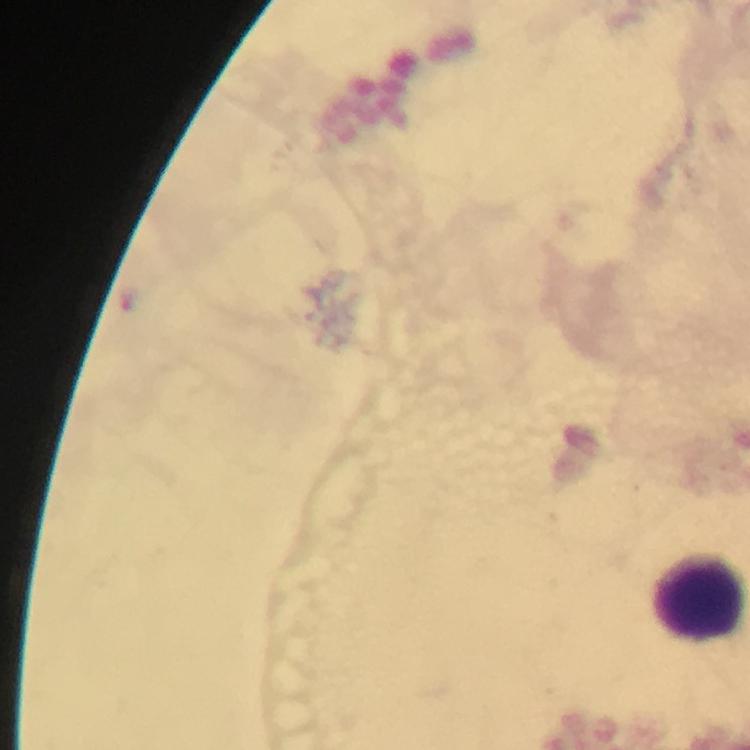
Approximate centers as (x, y) in pixels.
Summary:
  - Leukocyte locations: (699, 597)
  - Image size: 750×750 pixels
  - Capture: smartphone mounted on the microscope
  - Context: from a diagnostic examination for malaria
  - Preparation: thick smear
  - Cropped from: a single field of view
  - Malaria parasites: none detected
  - Stain: Giemsa
  - Immersion oil: used
  - Magnification: 100x